Classify this cell by malaria status.
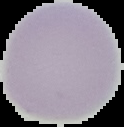

It is uninfected.

The area outside the segmented cell region is set to black. Image is 124×127 pixels. From a thin blood film.